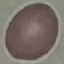
Malaria status: uninfected. Photographed with a smartphone camera at the microscope eyepiece. Giemsa stain. Thin blood film. Cell patch, automatically extracted from a larger field of view and resized to 64 × 64 pixels.